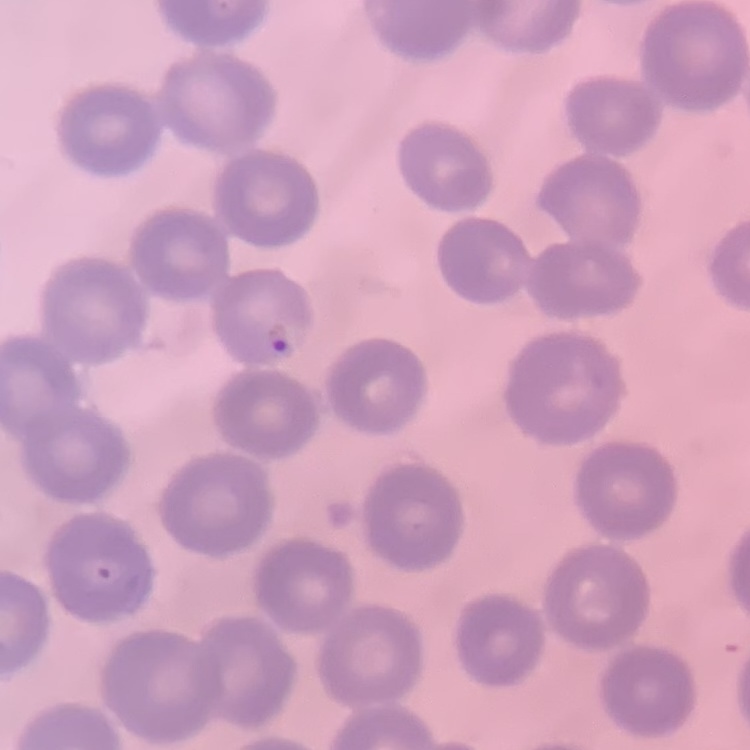 The red blood cells exhibit no rouleaux formation. Thin peripheral smear. One tile cut from a larger photomicrograph. Field's or Giemsa stain.